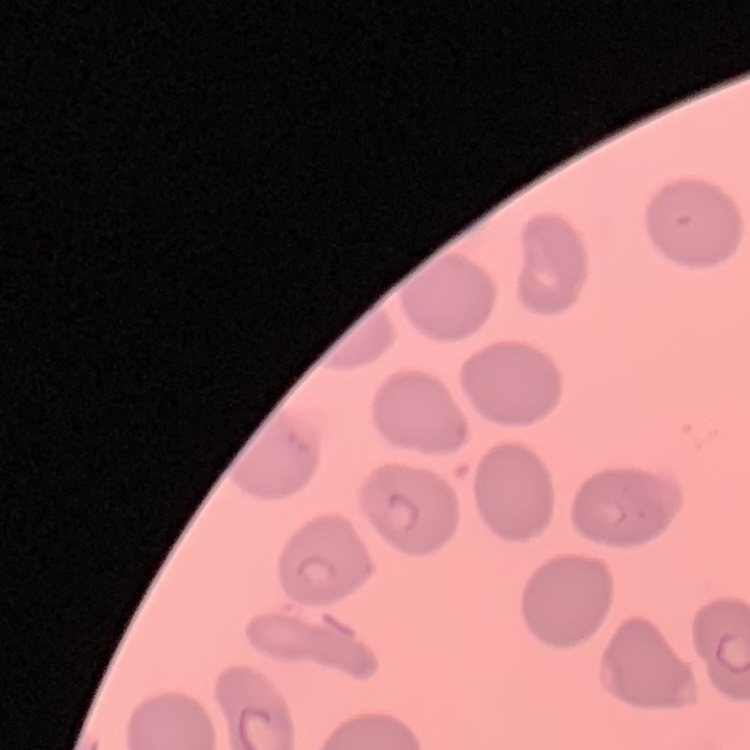
erythrocyte_morphology: no rouleaux formation
preparation: thin blood film
image_type: square crop of a larger photomicrograph
stain: Field's or Giemsa